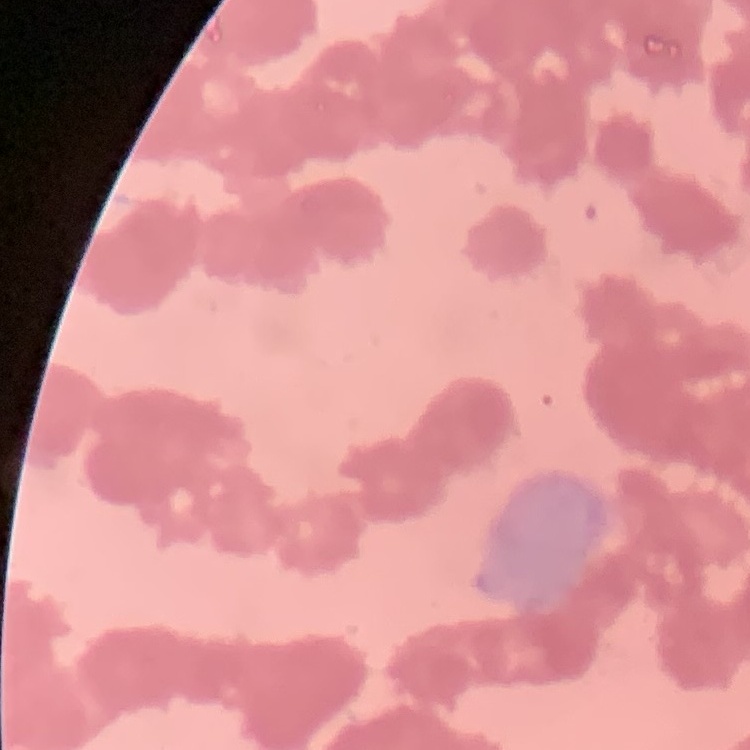

red_blood_cell_morphology: rouleaux formation
preparation: thin peripheral smear
image_type: one tile cut from a larger photomicrograph
stain: Field's or Giemsa